Point out leukocytes.
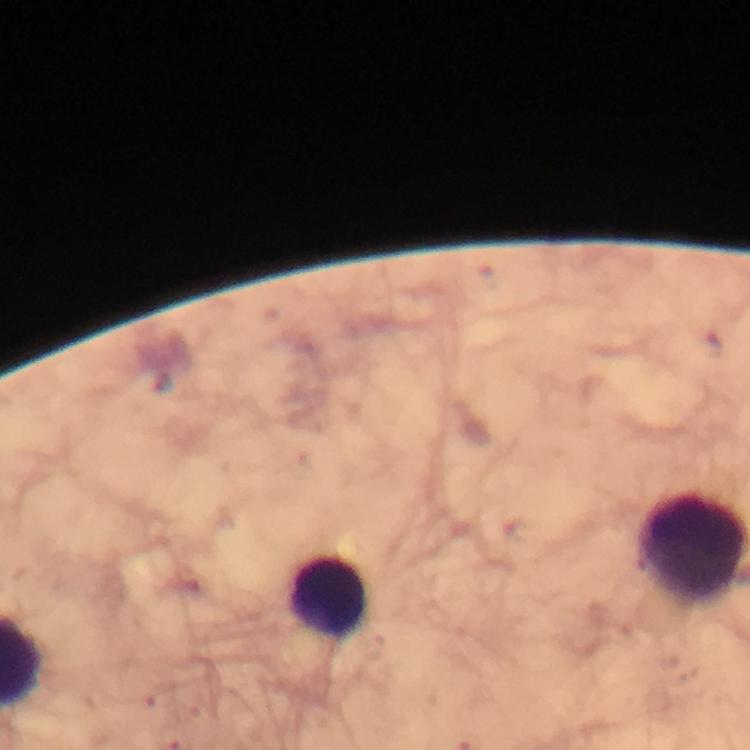
Approximate object centers, in pixels from the top-left corner.
Leukocytes: (x=329, y=596).

Summary:
  - Context: from a diagnostic examination for malaria
  - Magnification: 100x
  - Malaria parasites: none detected
  - Preparation: thick blood film
  - Image size: 750×750 pixels
  - Immersion oil: used
  - Capture: smartphone photograph through a microscope
  - Cropped from: one field of view
  - Stain: Giemsa